Report the malaria status of this cell.
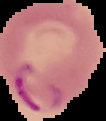
It is parasitized.

image type = cell region segmented out of the field of view; surrounding area masked to black
image size = 106×121 pixels
preparation = thin blood film